Assess the morphology of the red blood cells.
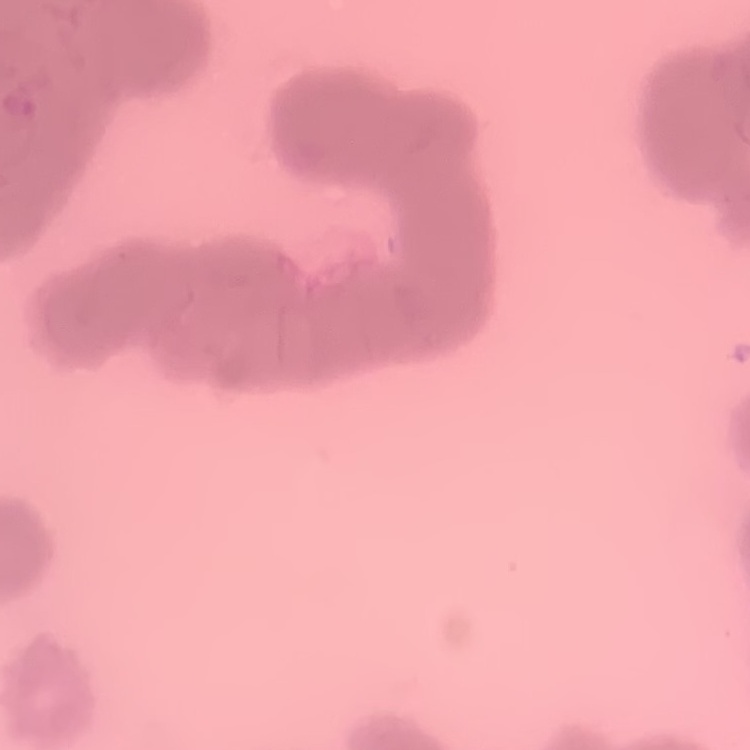
Rouleaux formation.

Stained with either Field's or Giemsa. Thin blood film. One tile cut from a larger photomicrograph.